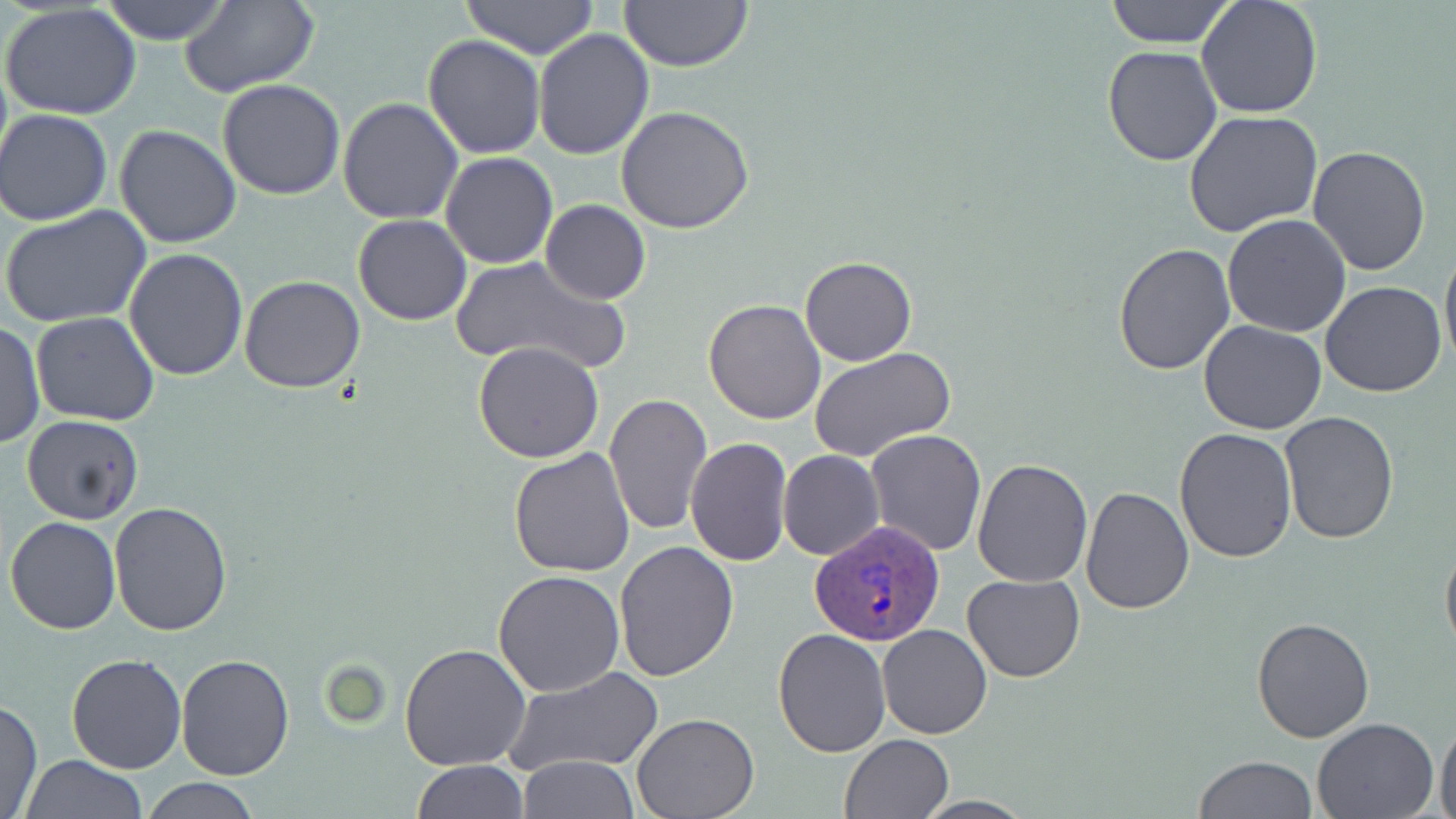

slide-level diagnosis = Plasmodium ovale
modality = optical microscopy
magnification = 1000x
field of view = one of a larger specimen
uninfected red blood cell locations = approximate bounding boxes as (x1,y1)-(x2,y2) corner pairs in pixels: (99,0)-(233,45), (459,0)-(600,57), (617,0)-(753,72), (1102,0)-(1237,48), (1196,0)-(1324,121), (178,2)-(319,95), (1,4)-(142,120), (532,28)-(655,159), (423,33)-(544,158), (1101,45)-(1223,166), (218,80)-(346,201), (337,96)-(464,225), (615,104)-(755,232), (1,108)-(116,225), (1183,110)-(1323,238), (113,124)-(240,249), (1308,145)-(1432,277), (441,152)-(559,269), (540,200)-(650,304), (1,204)-(153,328), (352,213)-(471,325), (1222,213)-(1351,338), (1440,235)-(1456,373), (1113,243)-(1234,375), (125,247)-(248,382), (448,255)-(630,377), (800,256)-(918,367), (238,274)-(365,392), (1320,281)-(1449,398), (703,298)-(827,424), (31,312)-(159,426), (1,319)-(44,451), (1199,321)-(1327,435), (472,341)-(605,463), (810,345)-(959,463), (604,392)-(713,536), (1280,411)-(1399,544), (22,416)-(144,525), (1173,426)-(1297,562), (864,428)-(986,556), (685,438)-(793,568), (509,448)-(636,578), (779,451)-(885,561), (972,459)-(1094,587), (1079,485)-(1194,613), (109,501)-(233,635), (5,517)-(123,635), (1440,530)-(1456,664), (613,541)-(739,682), (494,570)-(625,697), (961,573)-(1086,683), (1251,615)-(1377,742), (877,623)-(992,739), (772,627)-(890,759), (400,644)-(532,771), (65,653)-(188,774), (175,654)-(295,781), (502,665)-(665,777), (1,700)-(42,819), (631,713)-(760,819), (1313,717)-(1440,818), (1435,719)-(1456,819), (840,734)-(952,819), (20,755)-(148,818), (1194,755)-(1316,819), (518,756)-(640,817), (413,760)-(529,818), (139,777)-(261,817), (911,797)-(1038,818)
stain = May-Grünwald-Giemsa
image size = 1456×819 pixels
Plasmodium ovale-infected red blood cell locations = approximate bounding boxes as (x1,y1)-(x2,y2) corner pairs in pixels: (811,519)-(942,647)
preparation = thin blood smear